Assess the morphology of the red blood cells.
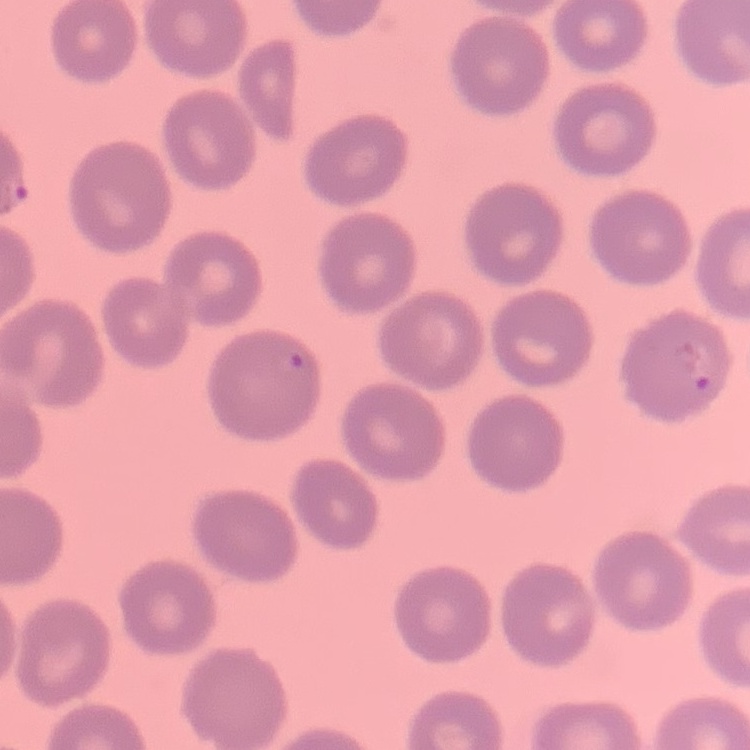

No rouleaux formation.

Summary:
  - Stain: Field's or Giemsa
  - Image type: one tile cut from a larger photomicrograph
  - Preparation: thin blood film